Report the malaria status of this cell.
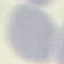
It is uninfected.

image_type: automatically extracted cell patch, resized to 64 × 64 pixels
stain: Giemsa
capture: smartphone through the microscope eyepiece
preparation: thin blood smear